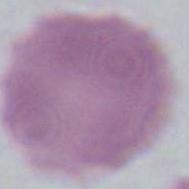
Summary:
  - Modality: micrograph
  - Magnification: 1000x
  - Identification: erythrocyte